Describe the morphology of the red blood cells.
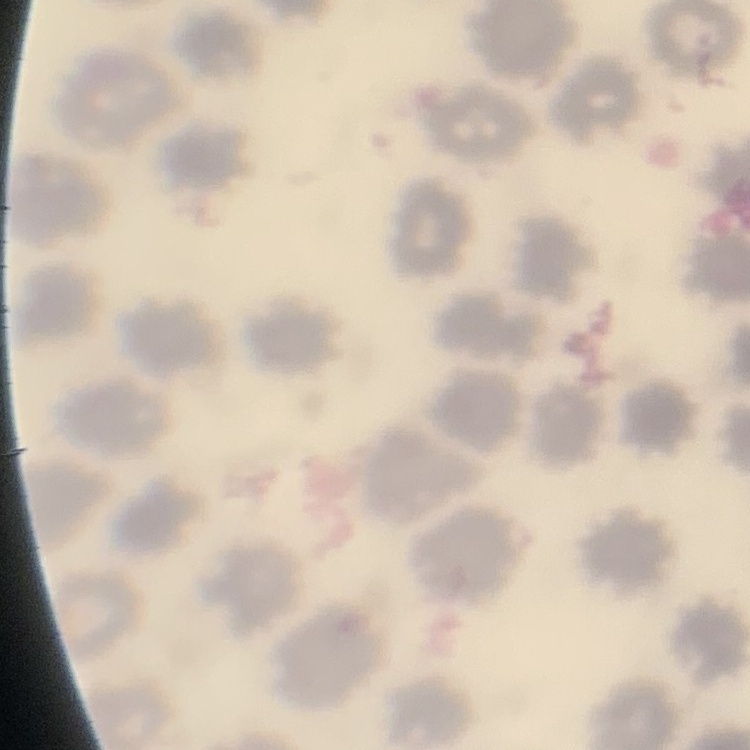
They show no rouleaux formation.

Field's or Giemsa stain. One tile cut from a larger photomicrograph. Thin blood smear.